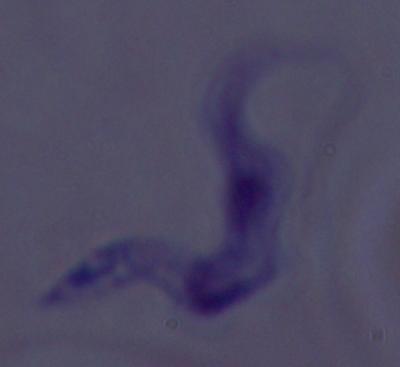

{
  "modality": "photomicrograph",
  "identification": "trypanosome",
  "magnification": "1000x"
}